Identify the parasite.
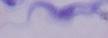
A trypanosome.

Captured at 1000x magnification. Micrograph.